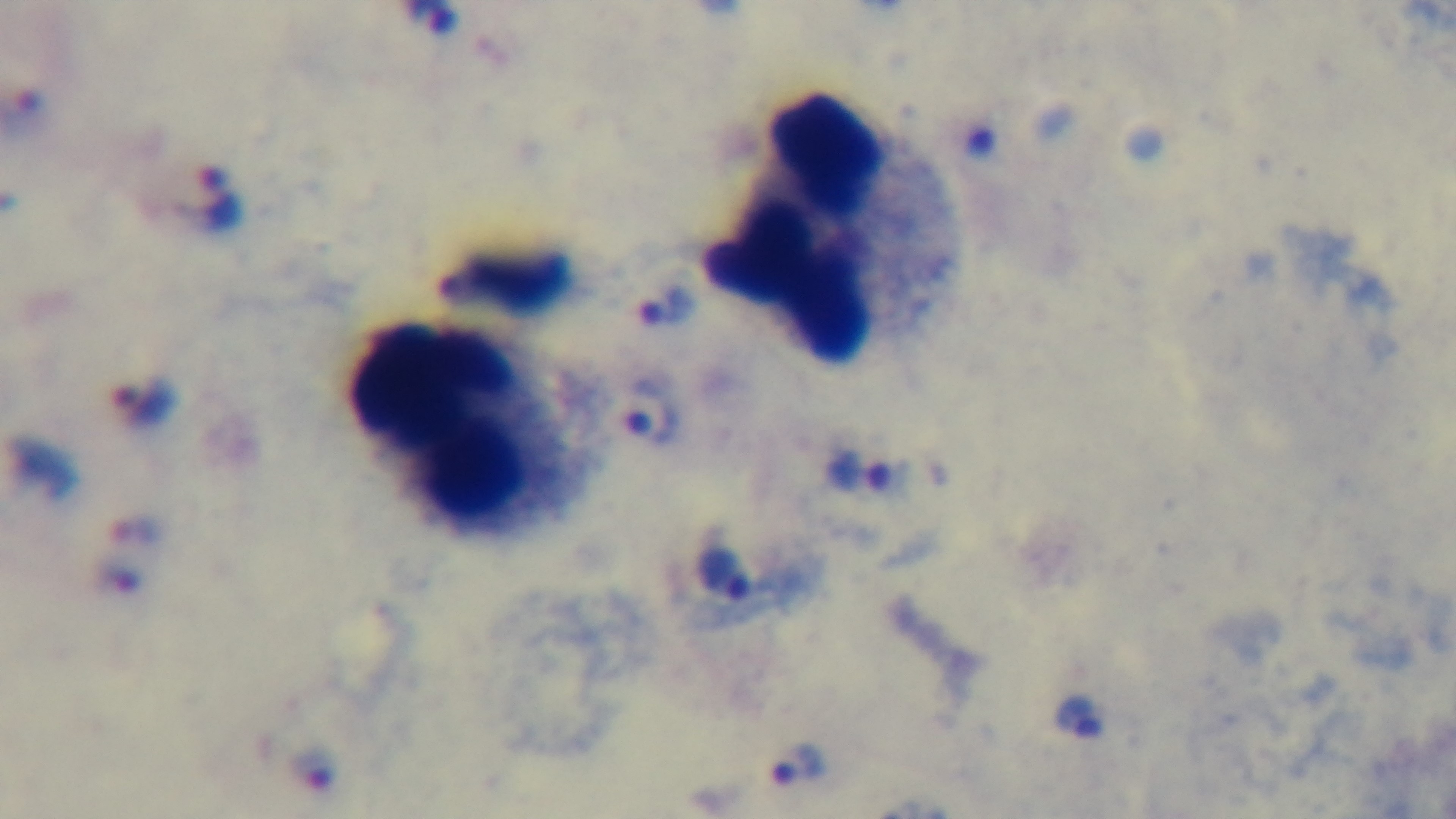

modality = light microscopy
objective = 100x oil immersion
capture = mounted 4K digital camera
stain = Giemsa
field of view = single
preparation = thick
malaria status = positive